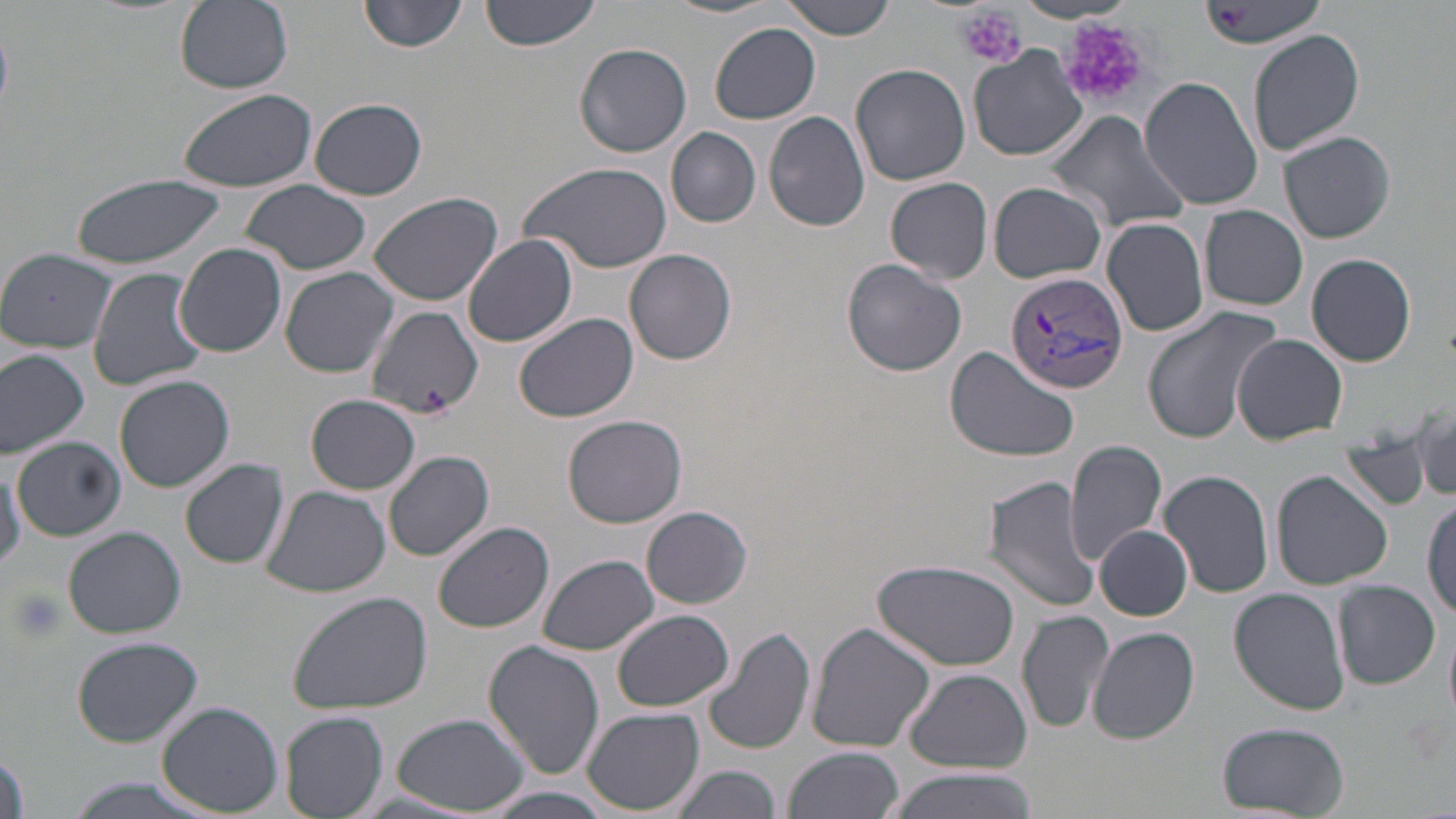

slide-level diagnosis = Plasmodium vivax
field of view = one of a larger specimen
platelet locations = approximate bounding boxes as (x1, y1, x2, y2) in pixels: (957, 5, 1026, 68), (1214, 5, 1249, 28), (1053, 14, 1149, 112), (421, 386, 451, 421), (5, 588, 67, 644)
magnification = 1000x
modality = light microscopy
Plasmodium vivax-infected red blood cell locations = approximate bounding boxes as (x1, y1, x2, y2) in pixels: (1005, 270, 1130, 394)
image size = 1456×819 pixels
stain = May-Grünwald-Giemsa
uninfected red blood cell locations = approximate bounding boxes as (x1, y1, x2, y2) in pixels: (174, 0, 293, 93), (357, 0, 470, 54), (481, 0, 601, 51), (665, 0, 782, 20), (783, 0, 897, 41), (1200, 0, 1322, 48), (709, 23, 822, 124), (1248, 28, 1362, 156), (575, 43, 692, 158), (968, 46, 1087, 162), (850, 62, 971, 186), (1139, 76, 1263, 210), (175, 87, 321, 192), (309, 97, 427, 200), (763, 111, 870, 232), (1046, 111, 1192, 235), (667, 127, 761, 227), (1279, 131, 1396, 243), (518, 158, 673, 274), (70, 170, 227, 270), (885, 176, 993, 284), (240, 179, 372, 275), (989, 182, 1107, 285), (366, 190, 503, 306), (1200, 207, 1309, 311), (1101, 216, 1210, 337), (463, 234, 578, 348), (175, 244, 286, 357), (625, 248, 736, 365), (0, 249, 117, 351), (1306, 252, 1418, 367), (841, 259, 968, 377), (87, 266, 210, 392), (278, 267, 400, 378), (1139, 304, 1281, 447), (366, 306, 482, 421), (515, 312, 637, 423), (1232, 333, 1348, 445), (946, 346, 1078, 460), (0, 349, 91, 458), (114, 374, 235, 493), (304, 393, 422, 495), (562, 414, 687, 527), (1417, 418, 1452, 497), (14, 438, 125, 539), (1341, 438, 1433, 512), (1065, 440, 1168, 566), (384, 450, 495, 561), (180, 457, 290, 568), (0, 459, 24, 571), (1157, 468, 1274, 598), (1271, 470, 1392, 590), (983, 475, 1101, 613), (261, 485, 390, 599), (1422, 493, 1455, 625), (642, 506, 753, 607), (433, 520, 554, 633), (1095, 526, 1192, 620), (63, 527, 185, 638), (538, 554, 658, 653), (874, 559, 1022, 672), (1333, 581, 1442, 690), (1229, 587, 1350, 717), (287, 589, 433, 714), (613, 609, 734, 712), (1016, 609, 1114, 735), (806, 623, 935, 754), (702, 625, 816, 759), (1088, 627, 1199, 744), (1444, 627, 1456, 723), (72, 635, 203, 747), (481, 638, 603, 782), (905, 668, 1030, 772), (157, 701, 283, 816), (583, 708, 706, 815), (280, 712, 388, 818), (392, 713, 532, 815), (1215, 721, 1349, 816), (782, 746, 905, 819), (671, 763, 783, 819), (879, 769, 1039, 819), (59, 777, 220, 819), (478, 788, 621, 819)
preparation = thin blood film